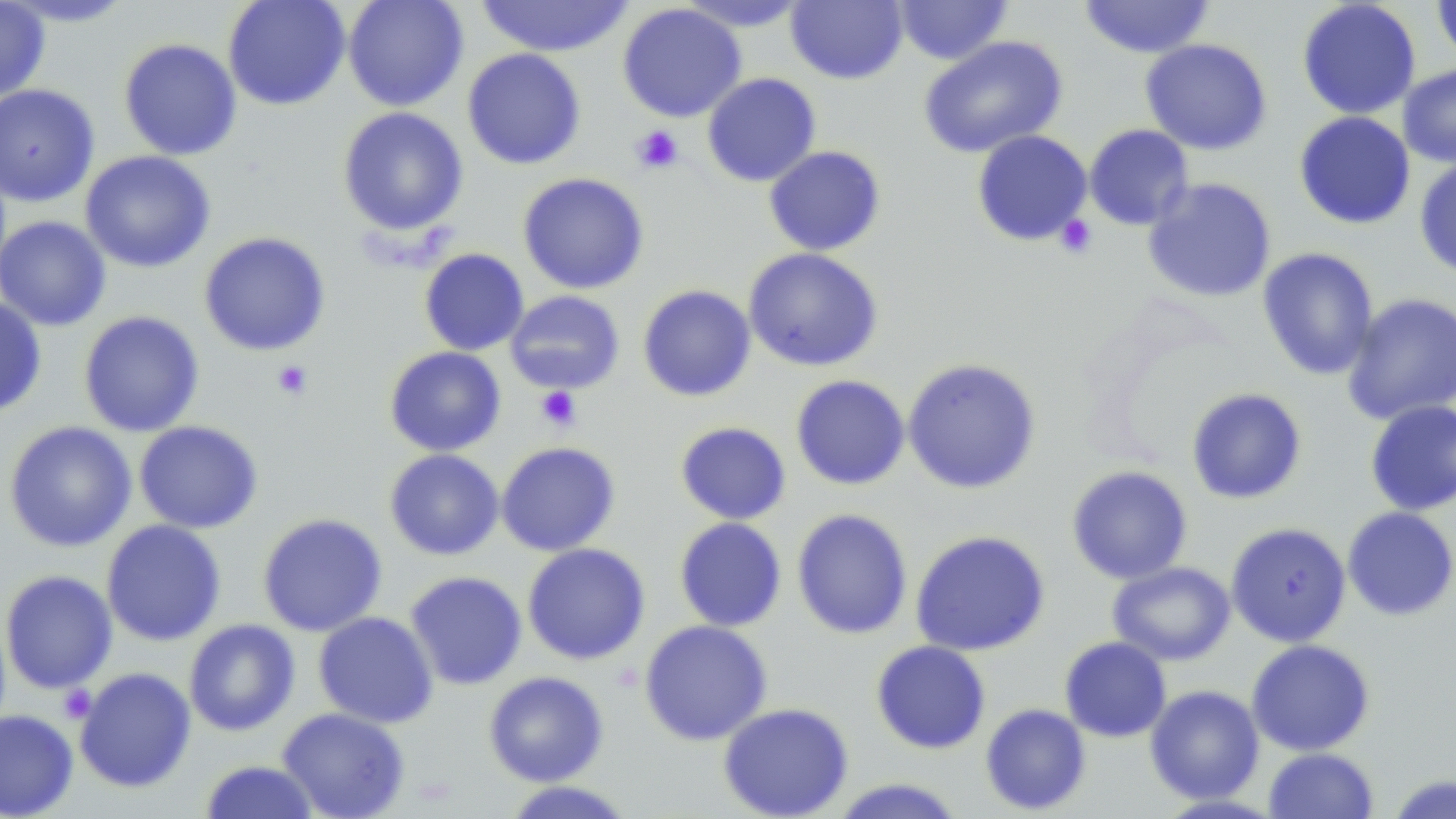

Summary:
  - Coordinate format: approximate bounding boxes as named x1/y1/x2/y2 corners in pixels
  - Platelet locations: (x1=631, y1=125, x2=684, y2=174), (x1=1054, y1=214, x2=1098, y2=258), (x1=271, y1=360, x2=314, y2=401), (x1=535, y1=386, x2=581, y2=432), (x1=58, y1=685, x2=97, y2=723)
  - Uninfected red blood cell locations: (x1=0, y1=0, x2=50, y2=103), (x1=2, y1=0, x2=139, y2=27), (x1=223, y1=0, x2=351, y2=111), (x1=342, y1=0, x2=468, y2=112), (x1=474, y1=0, x2=635, y2=57), (x1=786, y1=0, x2=908, y2=85), (x1=892, y1=0, x2=1013, y2=65), (x1=1079, y1=0, x2=1214, y2=59), (x1=1296, y1=0, x2=1421, y2=120), (x1=1432, y1=0, x2=1456, y2=68), (x1=675, y1=1, x2=813, y2=32), (x1=617, y1=3, x2=746, y2=123), (x1=918, y1=35, x2=1068, y2=159), (x1=119, y1=38, x2=242, y2=161), (x1=1140, y1=38, x2=1272, y2=155), (x1=462, y1=48, x2=586, y2=170), (x1=1398, y1=63, x2=1456, y2=169), (x1=702, y1=72, x2=821, y2=187), (x1=0, y1=84, x2=99, y2=206), (x1=337, y1=106, x2=469, y2=236), (x1=1293, y1=111, x2=1416, y2=230), (x1=1084, y1=124, x2=1195, y2=231), (x1=971, y1=130, x2=1093, y2=247), (x1=763, y1=145, x2=886, y2=256), (x1=80, y1=150, x2=216, y2=273), (x1=1413, y1=157, x2=1456, y2=279), (x1=518, y1=172, x2=649, y2=294), (x1=1142, y1=177, x2=1277, y2=303), (x1=0, y1=215, x2=111, y2=331), (x1=198, y1=231, x2=331, y2=356), (x1=742, y1=247, x2=884, y2=372), (x1=1257, y1=247, x2=1379, y2=381), (x1=419, y1=248, x2=529, y2=356), (x1=637, y1=284, x2=756, y2=402), (x1=505, y1=290, x2=625, y2=394), (x1=1341, y1=293, x2=1456, y2=425), (x1=0, y1=295, x2=48, y2=417), (x1=78, y1=311, x2=204, y2=437), (x1=384, y1=346, x2=506, y2=456), (x1=901, y1=357, x2=1042, y2=495), (x1=790, y1=375, x2=910, y2=490), (x1=1186, y1=387, x2=1307, y2=505), (x1=1364, y1=399, x2=1456, y2=516), (x1=133, y1=420, x2=263, y2=534), (x1=3, y1=421, x2=137, y2=553), (x1=674, y1=421, x2=791, y2=525), (x1=496, y1=441, x2=621, y2=556), (x1=384, y1=449, x2=504, y2=560), (x1=1066, y1=465, x2=1193, y2=584), (x1=1342, y1=506, x2=1456, y2=621), (x1=791, y1=508, x2=913, y2=640), (x1=257, y1=513, x2=387, y2=637), (x1=674, y1=517, x2=787, y2=632), (x1=101, y1=519, x2=226, y2=646), (x1=1225, y1=521, x2=1351, y2=647), (x1=910, y1=530, x2=1051, y2=656), (x1=522, y1=543, x2=651, y2=665), (x1=1107, y1=561, x2=1236, y2=666), (x1=0, y1=570, x2=118, y2=694), (x1=404, y1=571, x2=527, y2=690), (x1=313, y1=611, x2=438, y2=728), (x1=183, y1=619, x2=300, y2=736), (x1=639, y1=619, x2=772, y2=745), (x1=1060, y1=636, x2=1171, y2=742), (x1=1246, y1=639, x2=1375, y2=756), (x1=871, y1=640, x2=991, y2=754), (x1=74, y1=667, x2=196, y2=793), (x1=483, y1=671, x2=608, y2=786), (x1=1144, y1=685, x2=1265, y2=804), (x1=718, y1=702, x2=854, y2=818), (x1=980, y1=703, x2=1092, y2=815), (x1=276, y1=707, x2=410, y2=819), (x1=0, y1=709, x2=79, y2=818), (x1=1263, y1=747, x2=1379, y2=819), (x1=198, y1=760, x2=321, y2=819), (x1=1386, y1=774, x2=1456, y2=818), (x1=827, y1=778, x2=967, y2=818), (x1=500, y1=780, x2=638, y2=818)
  - Slide-level diagnosis: negative for blood parasites
  - Magnification: 1000x
  - Stain: May-Grünwald-Giemsa
  - Field of view: one of a larger specimen
  - Modality: optical microscopy
  - Preparation: thin blood film
  - Image size: 1456×819 pixels